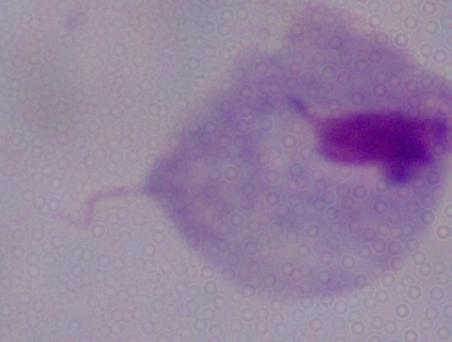
Summary:
  - Modality: photomicrograph
  - Identification: trichomonad
  - Magnification: 1000x